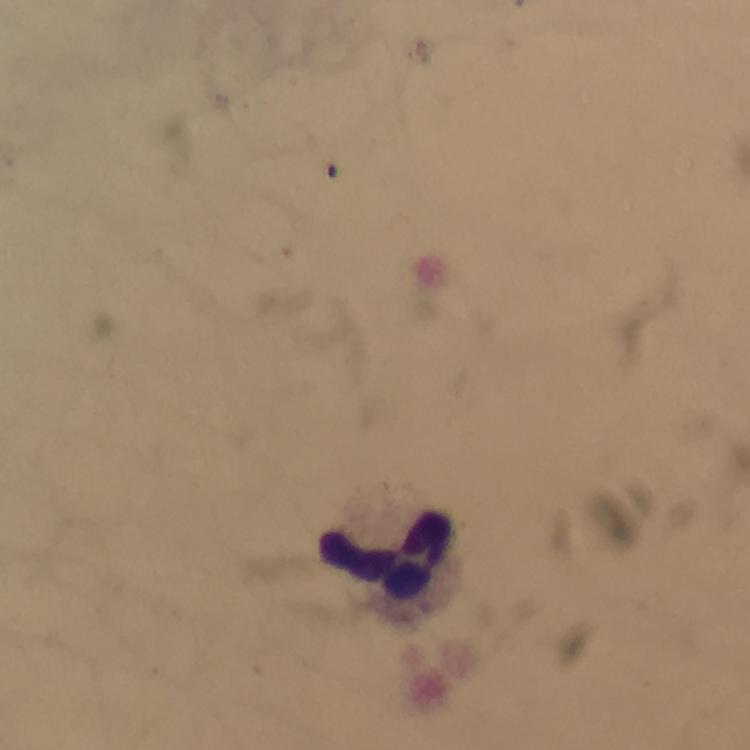
Approximate centers as (x, y) in pixels.
Summary:
  - Leukocyte locations: (389, 553)
  - Preparation: thick smear
  - Capture: smartphone mounted on the microscope
  - Immersion oil: applied
  - Image size: 750×750 pixels
  - Plasmodium parasites: none detected
  - Context: from a diagnostic examination for malaria
  - Stain: Giemsa
  - Cropped from: one field of view
  - Magnification: 100x